Name the parasite shown.
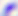

Toxoplasma gondii.

Photomicrograph. 400x magnification.